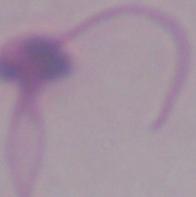

Summary:
  - Modality: micrograph
  - Identification: Leishmania
  - Magnification: 1000x